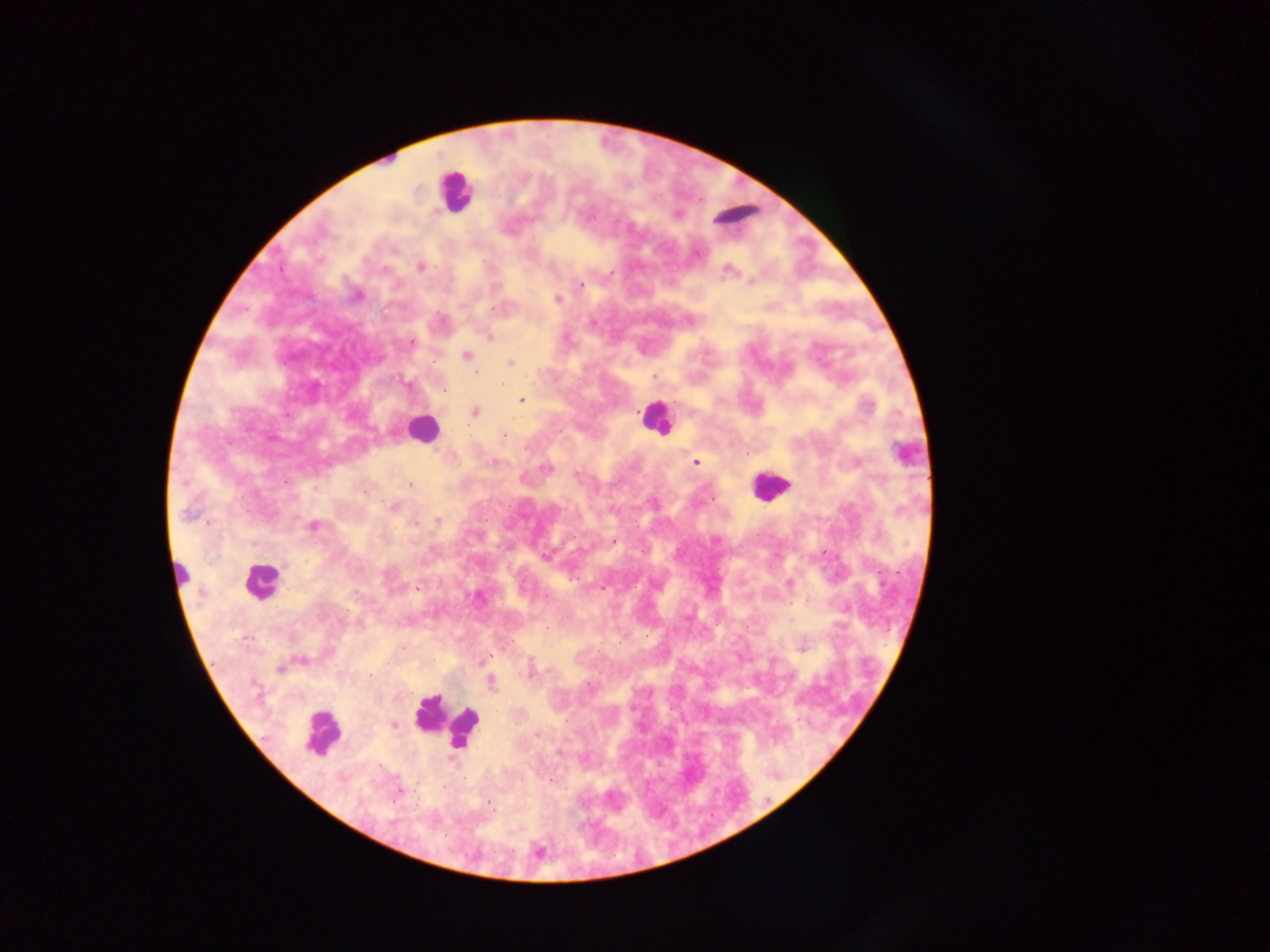

Approximate centers as [x, y] in pixels.
Summary:
  - Object labeled both malaria parasite and leukocyte by the source: [904, 453]
  - Leukocyte locations: [455, 190], [735, 215], [654, 417], [422, 429], [769, 485], [180, 574], [260, 581], [443, 722], [321, 734]
  - Malaria parasite locations: [394, 250], [420, 267], [385, 270], [728, 270], [752, 282], [580, 284], [357, 295], [557, 300], [493, 309], [489, 337], [411, 343], [467, 356], [510, 364], [476, 372], [654, 377], [444, 390], [522, 400], [475, 412], [504, 435], [696, 462], [545, 468], [576, 475], [410, 485], [393, 507], [188, 515], [437, 521], [415, 524], [313, 526], [613, 541], [544, 556], [417, 588], [546, 597], [803, 647], [486, 658], [300, 661], [281, 669], [531, 673], [492, 683], [588, 687], [393, 725], [538, 736], [559, 753], [398, 792], [489, 802]
  - Preparation: thick blood film
  - Field of view: single
  - Capture: mobile-phone photograph through a microscope
  - Image size: 1270×952 pixels
  - Country: Ghana